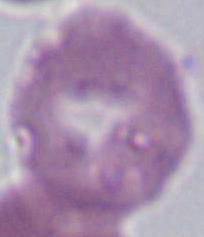
Micrograph. Captured at 1000x magnification. A red blood cell is seen.